Classify this cell by malaria status.
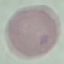

It is uninfected.

capture = smartphone camera at the microscope eyepiece
stain = Giemsa
image type = automatically extracted cell patch, resized to 64 × 64 pixels
preparation = thin blood film